Locate every blood parasite and identify its species.
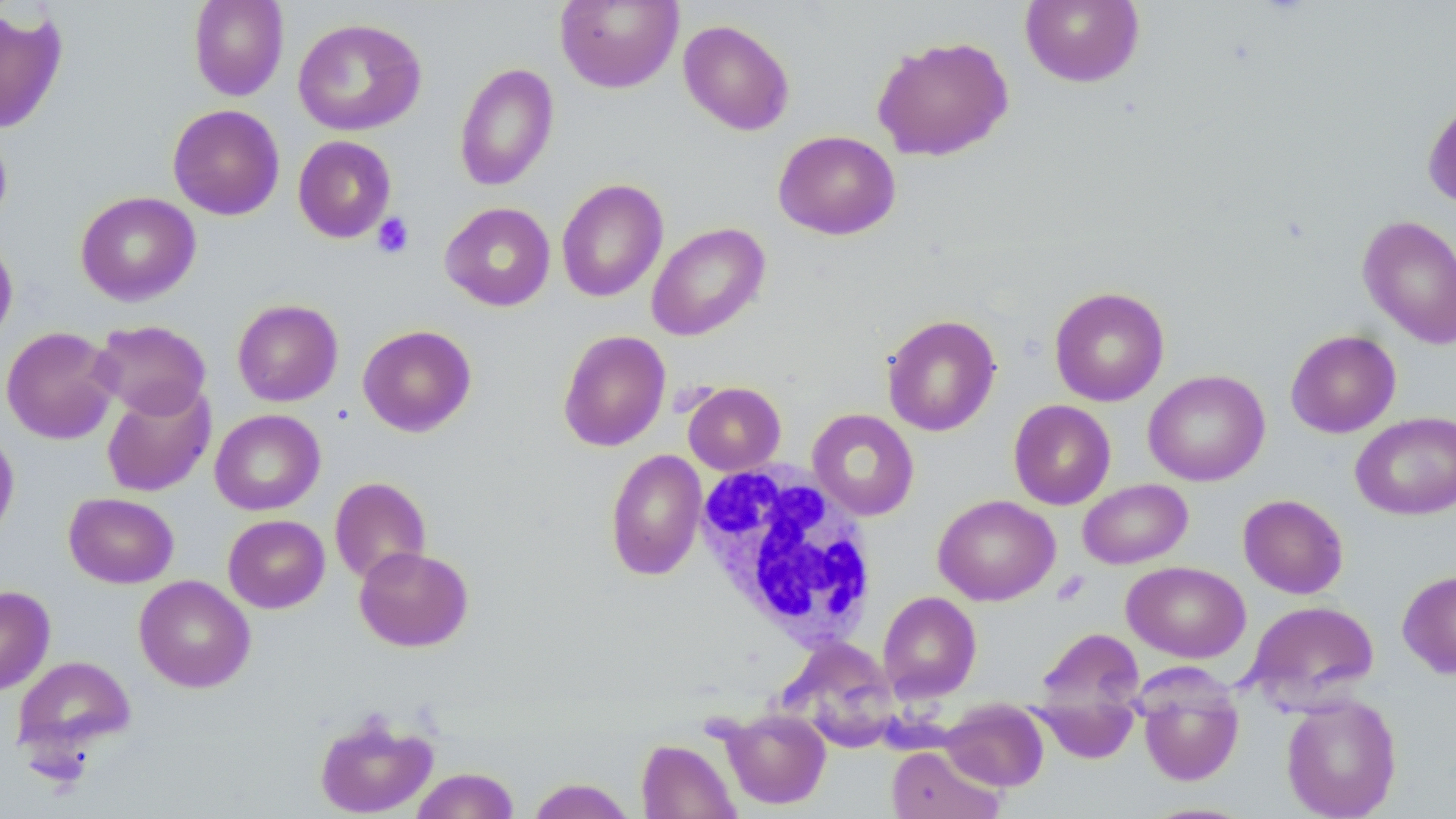

No blood parasites observed.

Approximate bounding boxes as named x1/y1/x2/y2 corners in pixels. White blood cell locations: (x1=693, y1=461, x2=879, y2=648). Platelet locations: (x1=372, y1=213, x2=415, y2=258). Uninfected red blood cell locations: (x1=189, y1=0, x2=289, y2=101), (x1=1020, y1=0, x2=1144, y2=88), (x1=555, y1=1, x2=683, y2=93), (x1=0, y1=8, x2=67, y2=134), (x1=293, y1=18, x2=426, y2=136), (x1=678, y1=19, x2=795, y2=136), (x1=871, y1=35, x2=1014, y2=162), (x1=454, y1=62, x2=559, y2=192), (x1=1422, y1=97, x2=1456, y2=211), (x1=167, y1=104, x2=285, y2=221), (x1=0, y1=128, x2=12, y2=229), (x1=773, y1=130, x2=900, y2=240), (x1=293, y1=135, x2=396, y2=242), (x1=556, y1=178, x2=668, y2=303), (x1=75, y1=191, x2=201, y2=306), (x1=440, y1=202, x2=555, y2=311), (x1=1358, y1=214, x2=1456, y2=348), (x1=646, y1=222, x2=770, y2=341), (x1=0, y1=235, x2=18, y2=346), (x1=1049, y1=286, x2=1170, y2=406), (x1=232, y1=299, x2=344, y2=406), (x1=882, y1=314, x2=1001, y2=436), (x1=91, y1=320, x2=211, y2=419), (x1=357, y1=324, x2=476, y2=437), (x1=1, y1=326, x2=121, y2=444), (x1=558, y1=329, x2=671, y2=452), (x1=1285, y1=330, x2=1401, y2=438), (x1=1143, y1=370, x2=1270, y2=487), (x1=683, y1=382, x2=786, y2=475), (x1=101, y1=384, x2=216, y2=497), (x1=1008, y1=400, x2=1116, y2=509), (x1=807, y1=408, x2=919, y2=520), (x1=210, y1=409, x2=326, y2=515), (x1=1351, y1=411, x2=1456, y2=520), (x1=0, y1=427, x2=19, y2=542), (x1=605, y1=449, x2=707, y2=580), (x1=329, y1=477, x2=431, y2=584), (x1=1078, y1=479, x2=1192, y2=569), (x1=64, y1=492, x2=179, y2=588), (x1=933, y1=494, x2=1060, y2=605), (x1=1238, y1=494, x2=1348, y2=599), (x1=223, y1=514, x2=330, y2=613), (x1=354, y1=546, x2=473, y2=652), (x1=1122, y1=561, x2=1250, y2=662), (x1=1397, y1=569, x2=1456, y2=679), (x1=134, y1=575, x2=255, y2=693), (x1=0, y1=585, x2=55, y2=695), (x1=877, y1=591, x2=982, y2=702), (x1=1244, y1=600, x2=1380, y2=711), (x1=1034, y1=628, x2=1144, y2=721), (x1=782, y1=638, x2=900, y2=752), (x1=12, y1=655, x2=136, y2=762), (x1=1137, y1=672, x2=1245, y2=787), (x1=1280, y1=693, x2=1402, y2=818), (x1=1031, y1=696, x2=1140, y2=764), (x1=941, y1=699, x2=1049, y2=792), (x1=721, y1=708, x2=831, y2=809), (x1=313, y1=712, x2=438, y2=817), (x1=636, y1=739, x2=740, y2=819), (x1=886, y1=745, x2=1003, y2=819), (x1=411, y1=767, x2=520, y2=819), (x1=527, y1=778, x2=635, y2=819). Slide-level diagnosis: negative for blood parasites. Optical microscopy. One field of a larger specimen. Thin blood smear. Image is 1456×819 pixels. May-Grünwald-Giemsa stain. Captured at 1000x magnification.